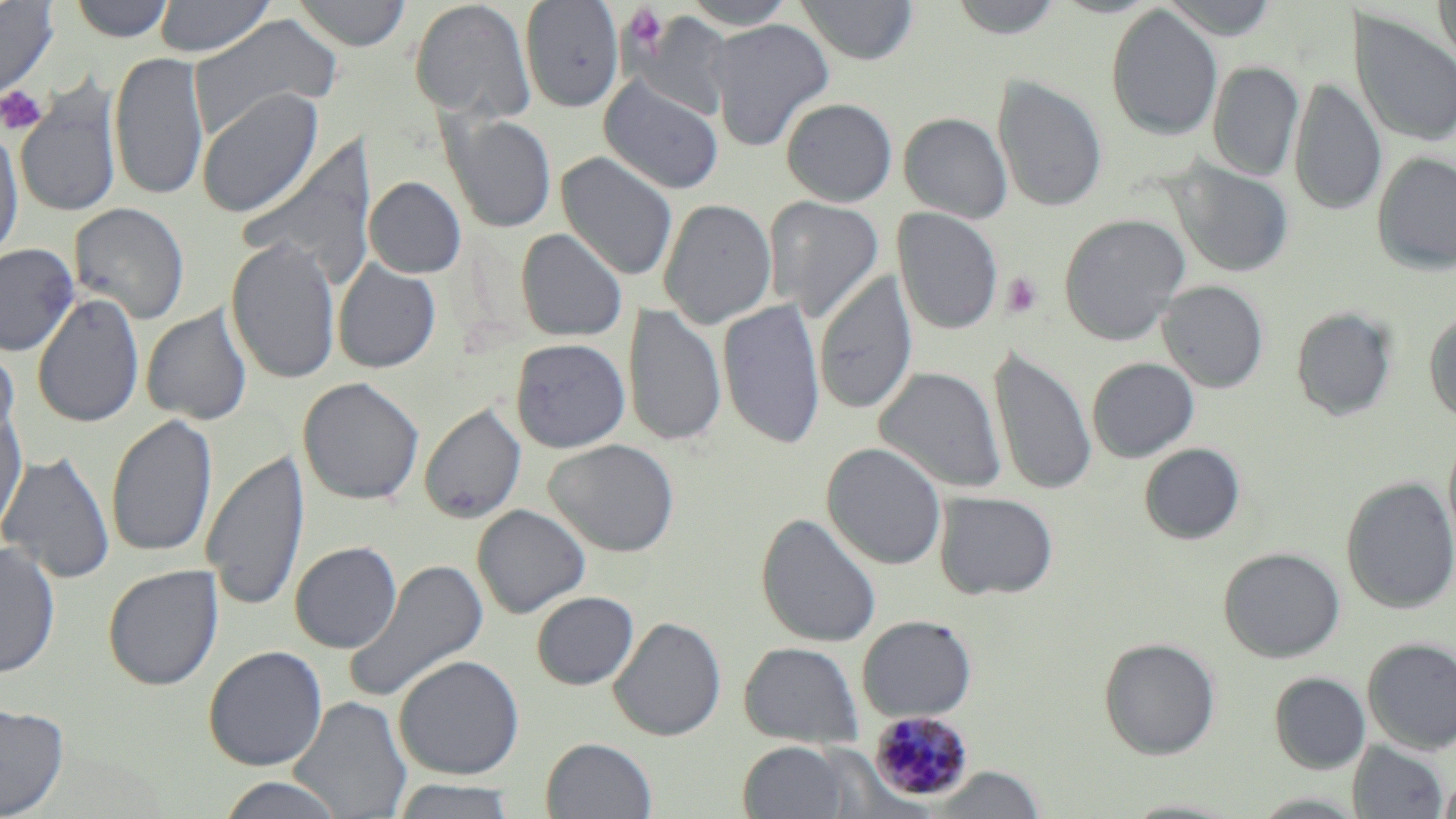
Summary:
  - Coordinate format: approximate bounding boxes as (x1,y1)-(x2,y2) corner pairs in pixels
  - Platelet locations: (622,5)-(670,54), (0,85)-(48,135), (1000,272)-(1044,320)
  - Plasmodium malariae-infected red blood cell locations: (868,710)-(973,803)
  - Uninfected red blood cell locations: (0,0)-(58,100), (69,0)-(176,42), (153,0)-(276,57), (292,0)-(412,51), (520,0)-(624,112), (680,0)-(799,29), (796,0)-(919,65), (948,0)-(1066,39), (1160,0)-(1280,40), (1434,0)-(1456,71), (409,1)-(536,124), (1105,5)-(1223,141), (1349,9)-(1456,148), (628,11)-(732,118), (188,14)-(343,137), (707,18)-(834,151), (109,51)-(209,201), (1207,61)-(1304,181), (993,75)-(1107,213), (599,76)-(723,194), (1289,77)-(1386,216), (14,83)-(122,219), (196,88)-(323,218), (781,97)-(898,206), (899,112)-(1012,223), (443,113)-(557,233), (0,124)-(24,265), (240,137)-(378,291), (556,151)-(678,281), (1372,152)-(1456,275), (1168,160)-(1295,278), (364,176)-(466,278), (765,195)-(885,321), (658,198)-(777,329), (69,202)-(190,324), (892,207)-(1003,336), (1058,213)-(1190,345), (515,228)-(628,342), (226,237)-(342,385), (0,243)-(79,357), (332,258)-(441,373), (814,270)-(918,416), (1158,280)-(1269,393), (32,293)-(145,429), (718,299)-(826,451), (623,302)-(726,449), (141,305)-(252,426), (1291,306)-(1398,421), (1424,309)-(1456,425), (510,338)-(630,453), (0,342)-(21,452), (990,346)-(1097,497), (1087,357)-(1199,462), (874,366)-(1007,495), (298,377)-(424,505), (420,403)-(526,524), (0,404)-(28,537), (106,413)-(218,560), (1444,431)-(1456,562), (544,438)-(680,557), (822,442)-(947,570), (1139,443)-(1246,545), (202,448)-(309,613), (0,450)-(116,585), (1341,477)-(1456,614), (934,491)-(1059,600), (472,504)-(590,618), (756,513)-(882,647), (289,541)-(403,653), (0,542)-(60,678), (1219,547)-(1345,663), (342,558)-(490,704), (102,565)-(223,690), (531,591)-(639,690), (856,615)-(977,723), (609,616)-(727,740), (1098,637)-(1220,759), (1362,638)-(1456,754), (739,641)-(863,749), (203,645)-(328,771), (393,654)-(524,780), (1269,672)-(1370,774), (289,696)-(412,819), (0,703)-(68,818), (541,737)-(657,818), (1348,740)-(1449,819), (738,741)-(851,819), (929,766)-(1046,818), (1438,771)-(1456,819), (215,776)-(348,818), (388,779)-(521,819), (1118,798)-(1247,818)
  - Slide-level diagnosis: Plasmodium malariae
  - Stain: May-Grünwald-Giemsa
  - Preparation: thin blood smear
  - Field of view: single
  - Modality: optical microscopy
  - Image size: 1456×819 pixels
  - Magnification: 1000x